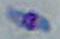

modality = photomicrograph
magnification = 1000x
identification = Toxoplasma gondii